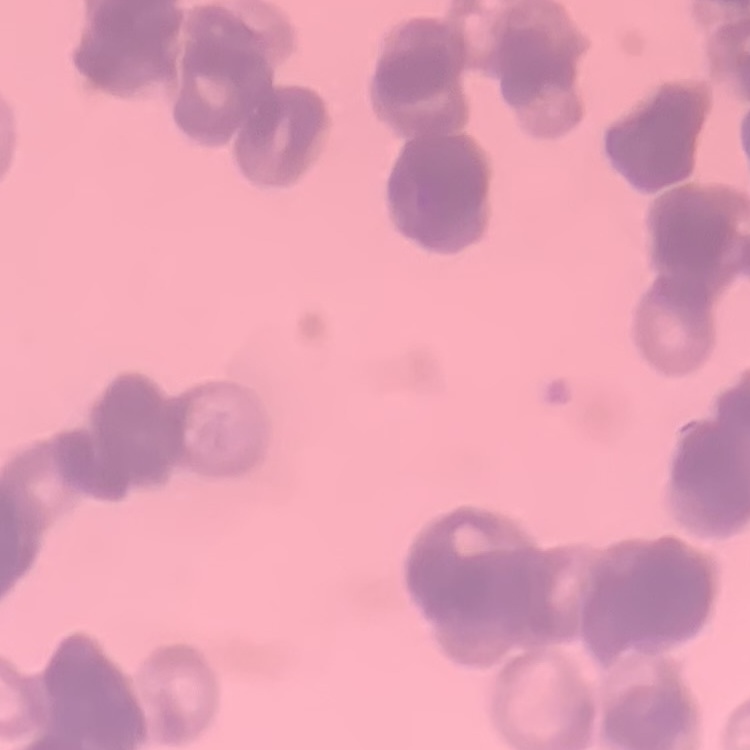
Summary:
  - Erythrocyte morphology: rouleaux formation
  - Preparation: thin blood film
  - Image type: square crop of a larger photomicrograph
  - Stain: Field's or Giemsa